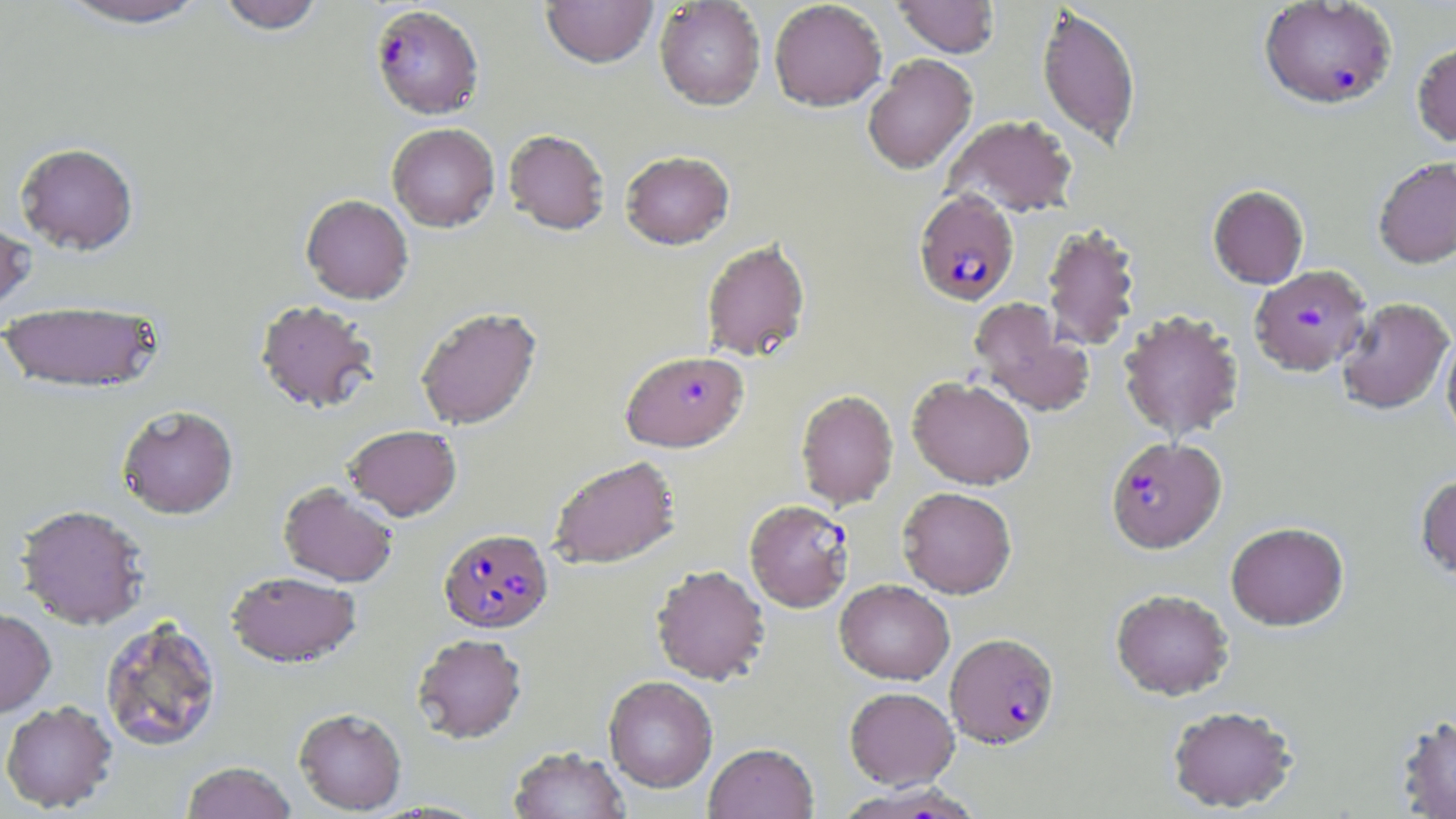

{
  "slide_level_diagnosis": "Plasmodium falciparum",
  "modality": "light microscopy",
  "preparation": "thin blood film",
  "stain": "May-Grünwald-Giemsa",
  "plasmodium_falciparum_infected_red_blood_cell_locations": "approximate bounding boxes as named x1/y1/x2/y2 corners in pixels: (x1=1258, y1=1, x2=1397, y2=110), (x1=370, y1=4, x2=484, y2=119), (x1=913, y1=190, x2=1019, y2=306), (x1=1249, y1=265, x2=1372, y2=376), (x1=621, y1=350, x2=749, y2=452), (x1=1105, y1=436, x2=1227, y2=553), (x1=744, y1=499, x2=855, y2=612), (x1=438, y1=527, x2=554, y2=633), (x1=945, y1=633, x2=1059, y2=748), (x1=839, y1=782, x2=985, y2=819)",
  "magnification": "1000x",
  "uninfected_red_blood_cell_locations": "approximate bounding boxes as named x1/y1/x2/y2 corners in pixels: (x1=54, y1=0, x2=213, y2=30), (x1=216, y1=0, x2=326, y2=35), (x1=769, y1=0, x2=887, y2=112), (x1=893, y1=0, x2=1000, y2=58), (x1=541, y1=1, x2=657, y2=69), (x1=654, y1=1, x2=765, y2=110), (x1=1036, y1=5, x2=1140, y2=149), (x1=1412, y1=40, x2=1456, y2=147), (x1=862, y1=53, x2=977, y2=174), (x1=943, y1=114, x2=1079, y2=217), (x1=387, y1=123, x2=499, y2=232), (x1=503, y1=129, x2=610, y2=235), (x1=15, y1=142, x2=139, y2=255), (x1=620, y1=150, x2=734, y2=250), (x1=1373, y1=157, x2=1456, y2=268), (x1=1207, y1=185, x2=1309, y2=289), (x1=301, y1=194, x2=413, y2=304), (x1=0, y1=218, x2=35, y2=317), (x1=1041, y1=222, x2=1142, y2=351), (x1=700, y1=239, x2=811, y2=362), (x1=1336, y1=297, x2=1454, y2=415), (x1=255, y1=299, x2=380, y2=414), (x1=969, y1=299, x2=1093, y2=417), (x1=0, y1=300, x2=165, y2=395), (x1=415, y1=306, x2=542, y2=430), (x1=1118, y1=309, x2=1244, y2=442), (x1=1441, y1=332, x2=1456, y2=446), (x1=907, y1=376, x2=1036, y2=490), (x1=795, y1=389, x2=899, y2=509), (x1=117, y1=405, x2=238, y2=519), (x1=343, y1=424, x2=462, y2=521), (x1=547, y1=455, x2=681, y2=569), (x1=1415, y1=474, x2=1456, y2=584), (x1=278, y1=482, x2=398, y2=587), (x1=898, y1=486, x2=1017, y2=599), (x1=15, y1=503, x2=150, y2=629), (x1=1225, y1=521, x2=1349, y2=631), (x1=651, y1=564, x2=770, y2=685), (x1=225, y1=570, x2=361, y2=668), (x1=834, y1=579, x2=955, y2=685), (x1=1110, y1=588, x2=1234, y2=701), (x1=0, y1=607, x2=56, y2=718), (x1=99, y1=615, x2=223, y2=753), (x1=412, y1=633, x2=527, y2=744), (x1=603, y1=675, x2=718, y2=792), (x1=845, y1=686, x2=958, y2=789), (x1=0, y1=700, x2=118, y2=812), (x1=1166, y1=704, x2=1298, y2=813), (x1=294, y1=707, x2=407, y2=814), (x1=1395, y1=713, x2=1456, y2=819), (x1=704, y1=742, x2=818, y2=819), (x1=508, y1=746, x2=631, y2=819), (x1=181, y1=761, x2=297, y2=819)",
  "field_of_view": "single",
  "image_size": "1456×819 pixels"
}